Identify the cell.
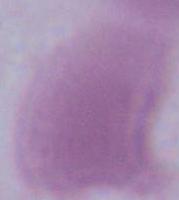

An erythrocyte.

Summary:
  - Modality: photomicrograph
  - Magnification: 1000x